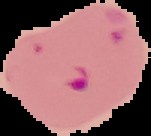

Summary:
  - Result: malaria parasites identified
  - Preparation: thin blood smear
  - Image type: cell region segmented out of the field of view; surrounding area masked to black
  - Image size: 151×136 pixels